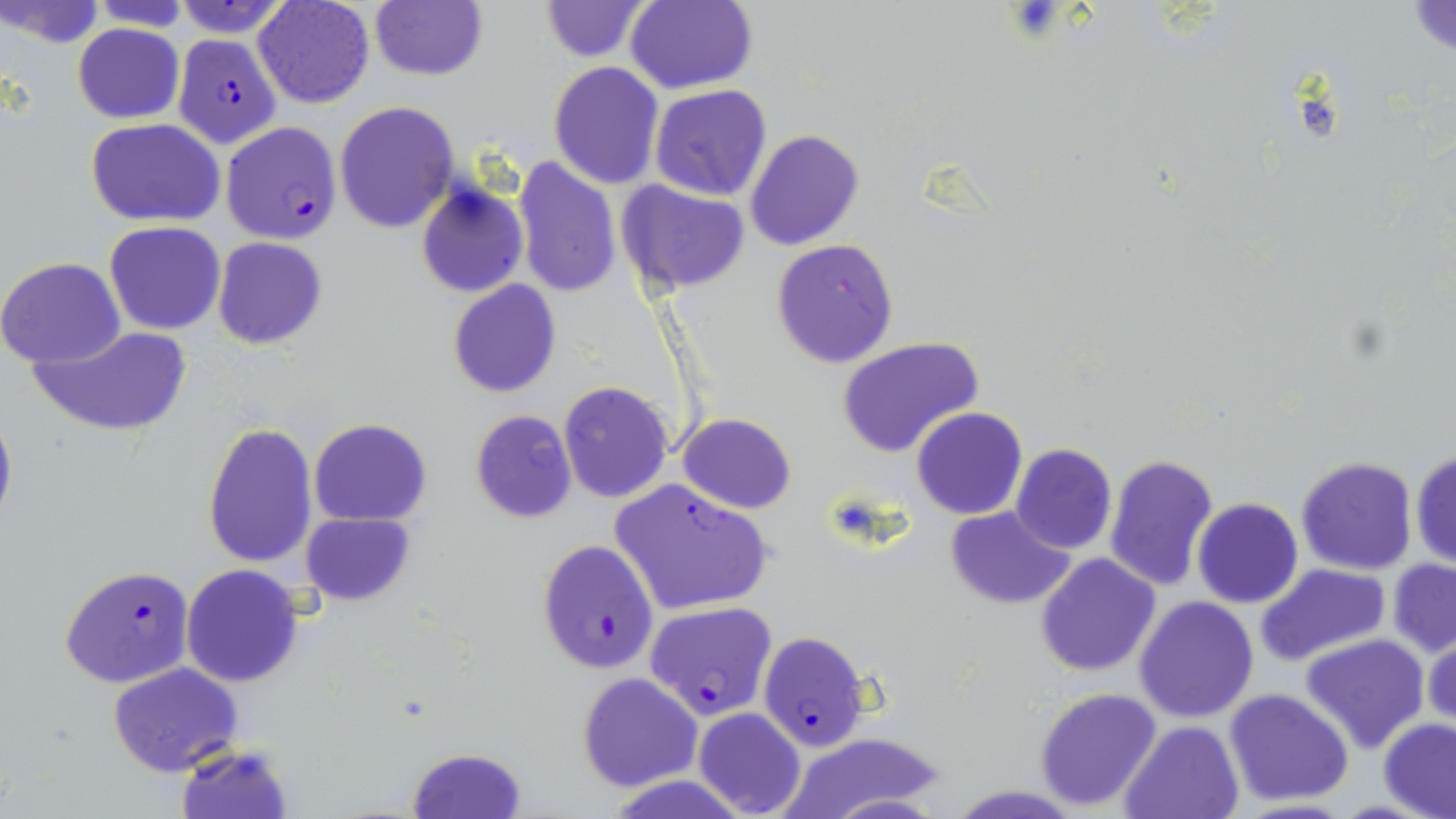

Approximate bounding boxes as (x1, y1, x2, y2) in pixels. Plasmodium falciparum-infected red blood cell locations: (171, 32, 285, 146), (221, 121, 344, 245), (610, 478, 775, 615), (536, 539, 659, 673), (60, 566, 196, 687), (645, 602, 779, 719), (758, 631, 873, 751). Platelet locations: (1004, 1, 1071, 44). Uninfected red blood cell locations: (1, 0, 104, 47), (87, 0, 197, 32), (173, 0, 294, 36), (253, 0, 376, 109), (370, 0, 487, 81), (537, 0, 652, 62), (623, 2, 756, 91), (1406, 3, 1454, 56), (72, 23, 185, 123), (547, 61, 665, 189), (650, 85, 774, 201), (334, 100, 457, 233), (85, 118, 226, 226), (744, 128, 866, 251), (511, 155, 621, 298), (616, 181, 751, 296), (415, 182, 528, 298), (104, 221, 226, 335), (211, 236, 328, 348), (771, 238, 899, 370), (0, 257, 127, 369), (448, 280, 562, 399), (31, 323, 192, 437), (837, 336, 986, 460), (557, 381, 672, 503), (0, 397, 17, 537), (911, 407, 1028, 520), (469, 409, 577, 524), (677, 413, 796, 513), (310, 417, 433, 526), (202, 421, 318, 568), (1010, 444, 1117, 554), (1410, 447, 1456, 570), (1102, 453, 1220, 593), (1295, 455, 1418, 574), (1192, 498, 1303, 608), (944, 507, 1076, 608), (302, 511, 414, 606), (1034, 553, 1162, 677), (1388, 559, 1456, 657), (1257, 563, 1387, 666), (181, 564, 304, 687), (1133, 595, 1258, 723), (1423, 629, 1455, 730), (1301, 633, 1431, 755), (106, 663, 244, 777), (577, 673, 703, 793), (1034, 687, 1163, 812), (1225, 688, 1353, 805), (695, 708, 805, 818), (1378, 717, 1456, 819), (1121, 719, 1243, 819), (775, 732, 953, 818), (174, 742, 292, 818), (407, 747, 524, 818), (609, 776, 749, 818), (947, 784, 1083, 817). Slide-level diagnosis: Plasmodium falciparum. Optical microscopy. One field of a larger specimen. Thin blood smear. Image is 1456×819 pixels. 1000x magnification. May-Grünwald-Giemsa stain.